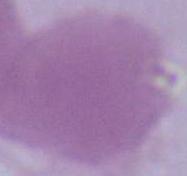

Summary:
  - Modality: micrograph
  - Magnification: 1000x
  - Identification: red blood cell